Comment on the morphology of the erythrocytes.
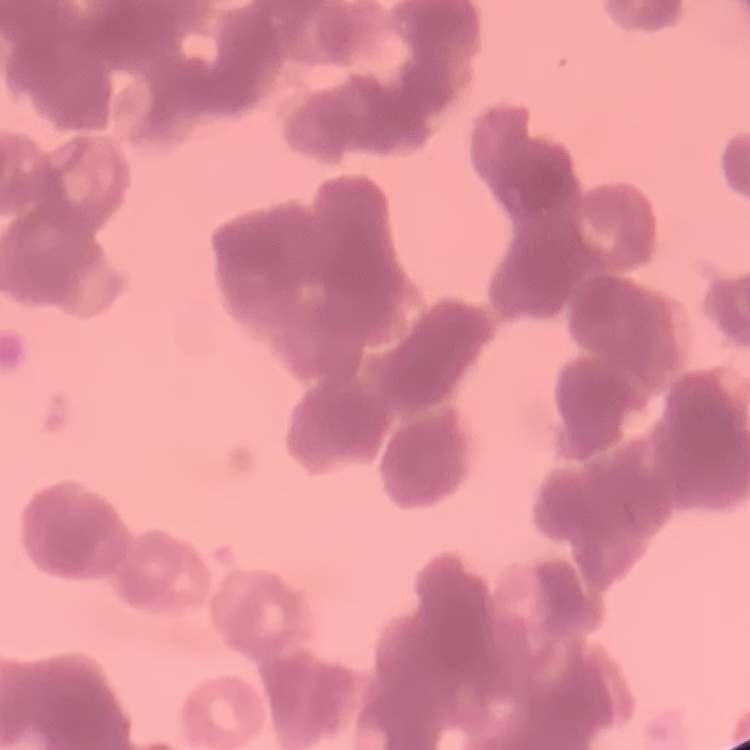
Rouleaux formation.

Summary:
  - Preparation: thin peripheral smear
  - Stain: Field's or Giemsa
  - Image type: one tile cut from a larger photomicrograph